Describe the morphology of the red blood cells.
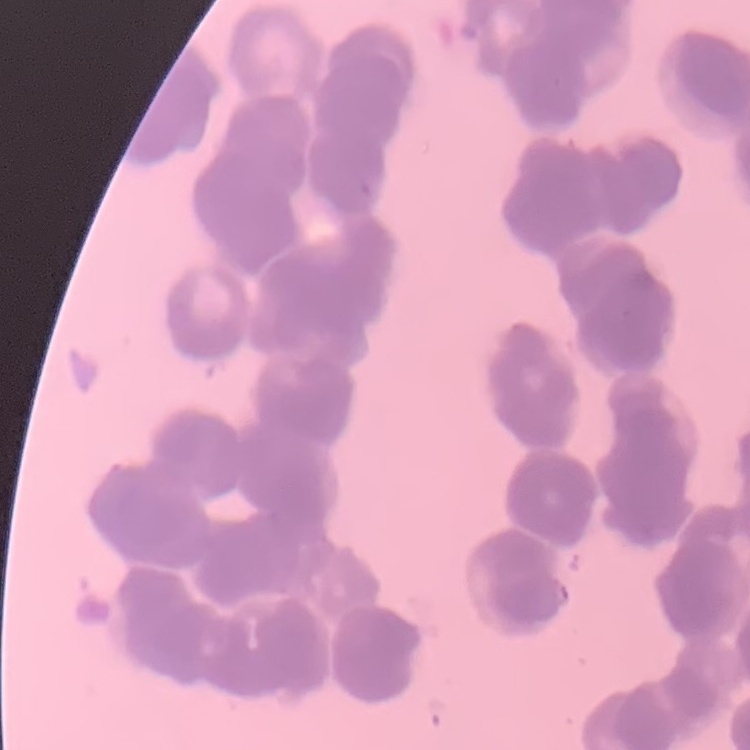

They show rouleaux formation.

stain = Field's or Giemsa
preparation = thin blood smear
image type = one tile cut from a larger photomicrograph